Give the preparation type.
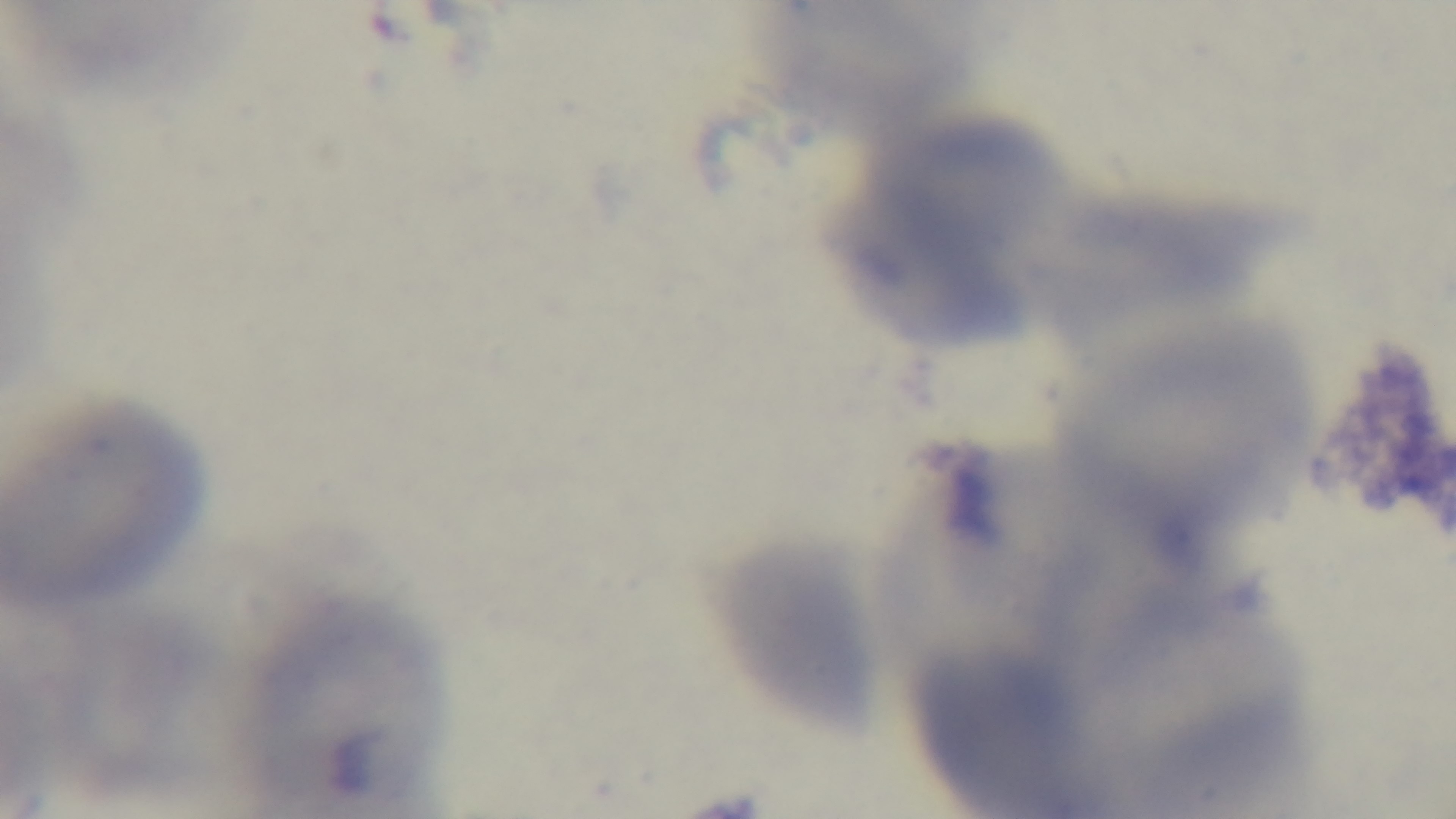
It is a thin blood film.

Summary:
  - Malaria status: uninfected
  - Modality: light microscopy
  - Field of view: single
  - Capture: mounted 4K digital camera
  - Objective: 100x oil immersion
  - Stain: Giemsa